Classify this cell by malaria status.
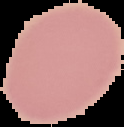
Uninfected.

Summary:
  - Preparation: thin blood smear
  - Image size: 124×127 pixels
  - Image type: segmented cell region with the area outside set to black